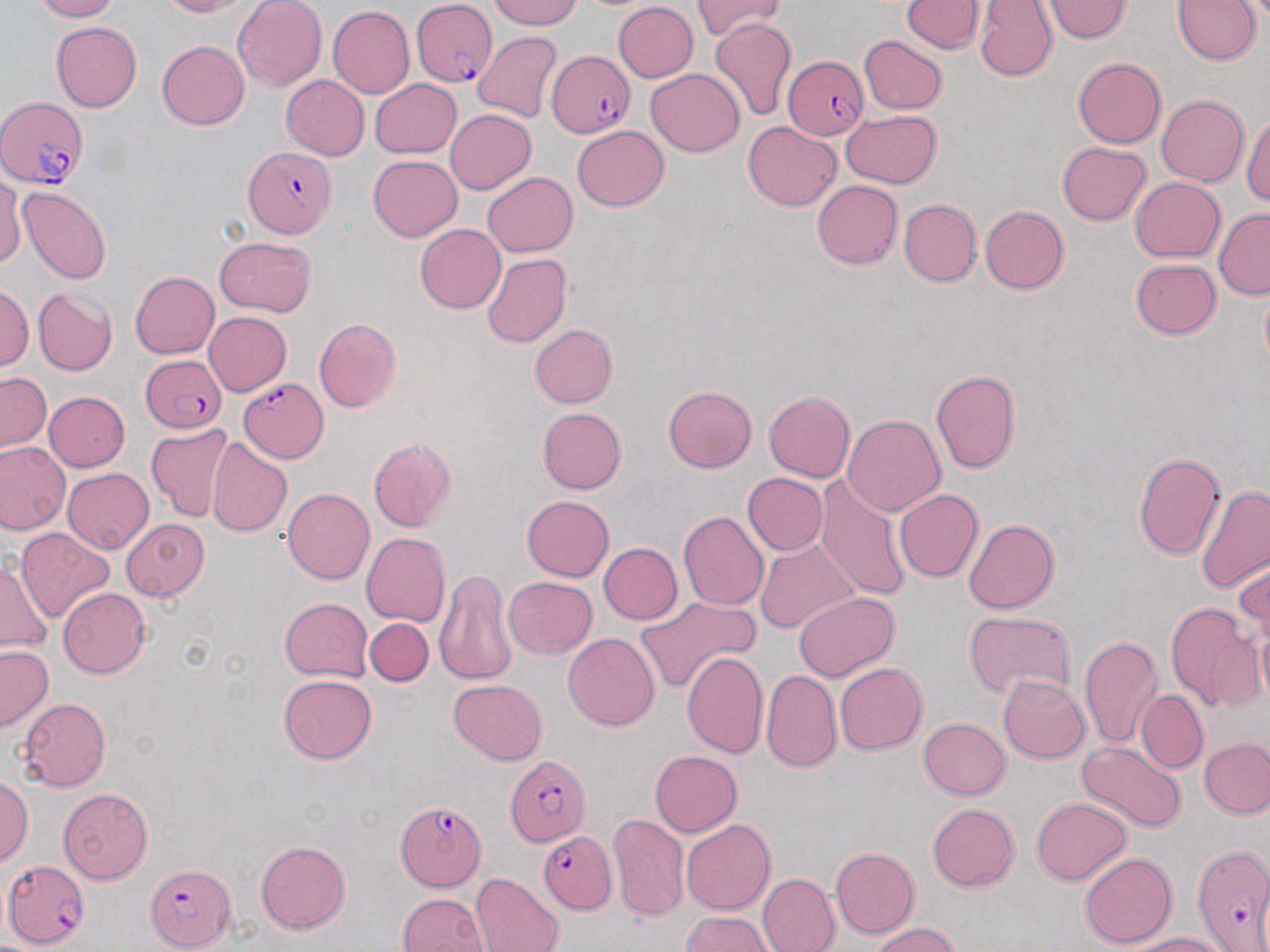

Summary:
  - Coordinate format: approximate bounding boxes as (x1,y1)-(x2,y2) corner pairs in pixels
  - Uninfected red blood cell locations: (29,0)-(118,22), (157,0)-(251,18), (234,0)-(327,92), (489,0)-(582,28), (692,0)-(786,41), (901,0)-(984,52), (975,0)-(1058,82), (1043,0)-(1133,42), (1172,1)-(1260,66), (613,2)-(698,82), (327,5)-(414,99), (709,17)-(797,121), (51,21)-(141,112), (472,31)-(564,122), (860,35)-(947,114), (156,40)-(249,130), (1072,57)-(1165,147), (646,69)-(745,156), (281,76)-(369,159), (370,79)-(462,158), (1147,94)-(1236,265), (1156,94)-(1249,186), (444,109)-(537,195), (841,110)-(942,189), (1242,114)-(1270,205), (742,121)-(841,211), (572,125)-(669,211), (1057,142)-(1152,226), (368,155)-(462,242), (482,172)-(578,257), (1131,176)-(1226,261), (0,177)-(25,268), (811,181)-(902,270), (15,186)-(112,284), (899,198)-(982,286), (980,206)-(1069,294), (1213,208)-(1270,300), (416,224)-(506,313), (215,235)-(316,317), (482,252)-(572,348), (1131,258)-(1220,339), (131,271)-(221,359), (0,285)-(32,370), (34,288)-(117,376), (205,311)-(292,396), (313,318)-(401,412), (529,324)-(617,407), (930,369)-(1020,474), (1,372)-(51,451), (663,385)-(757,473), (43,391)-(130,471), (763,391)-(856,482), (537,407)-(626,494), (843,414)-(945,516), (147,423)-(233,523), (368,437)-(458,533), (207,438)-(292,537), (0,442)-(70,534), (1133,451)-(1227,560), (63,467)-(153,554), (741,472)-(828,556), (815,476)-(914,603), (1196,484)-(1270,596), (282,488)-(375,584), (895,489)-(984,582), (521,494)-(614,581), (678,511)-(769,611), (121,519)-(210,600), (964,519)-(1059,613), (15,528)-(115,622), (361,532)-(450,627), (754,539)-(859,635), (598,542)-(682,624), (1234,557)-(1269,648), (0,560)-(52,653), (434,568)-(517,686), (503,576)-(597,658), (58,587)-(151,678), (794,592)-(900,681), (636,595)-(760,695), (279,598)-(372,680), (1163,602)-(1264,715), (963,610)-(1077,701), (364,618)-(433,687), (563,632)-(659,731), (1077,633)-(1162,750), (0,645)-(53,732), (681,649)-(769,759), (835,662)-(927,755), (761,669)-(842,773), (279,674)-(378,763), (998,675)-(1090,763), (448,679)-(547,765), (1136,690)-(1208,774), (16,698)-(112,790), (917,717)-(1010,799), (1200,739)-(1270,819), (1077,740)-(1188,833), (650,750)-(742,836), (0,776)-(33,867), (57,788)-(152,884), (1031,796)-(1131,885), (926,803)-(1020,891), (608,813)-(689,924), (680,819)-(775,916), (256,840)-(351,934), (831,847)-(920,938), (1079,852)-(1178,949), (757,860)-(916,946), (471,872)-(565,952), (757,872)-(840,952), (398,893)-(489,952), (681,912)-(774,951), (870,923)-(962,952), (1124,932)-(1226,952)
  - Plasmodium falciparum-infected red blood cell locations: (412,2)-(496,87), (547,49)-(633,138), (783,56)-(870,141), (1,96)-(89,187), (243,146)-(337,240), (140,355)-(226,432), (241,377)-(330,461), (506,754)-(590,846), (393,799)-(485,892), (538,830)-(617,914), (3,860)-(90,949), (146,864)-(236,949)
  - Slide-level diagnosis: Plasmodium falciparum
  - Preparation: thin blood smear
  - Field of view: one of a larger specimen
  - Stain: May-Grünwald-Giemsa
  - Magnification: 1000x
  - Image size: 1270×952 pixels
  - Modality: optical microscopy